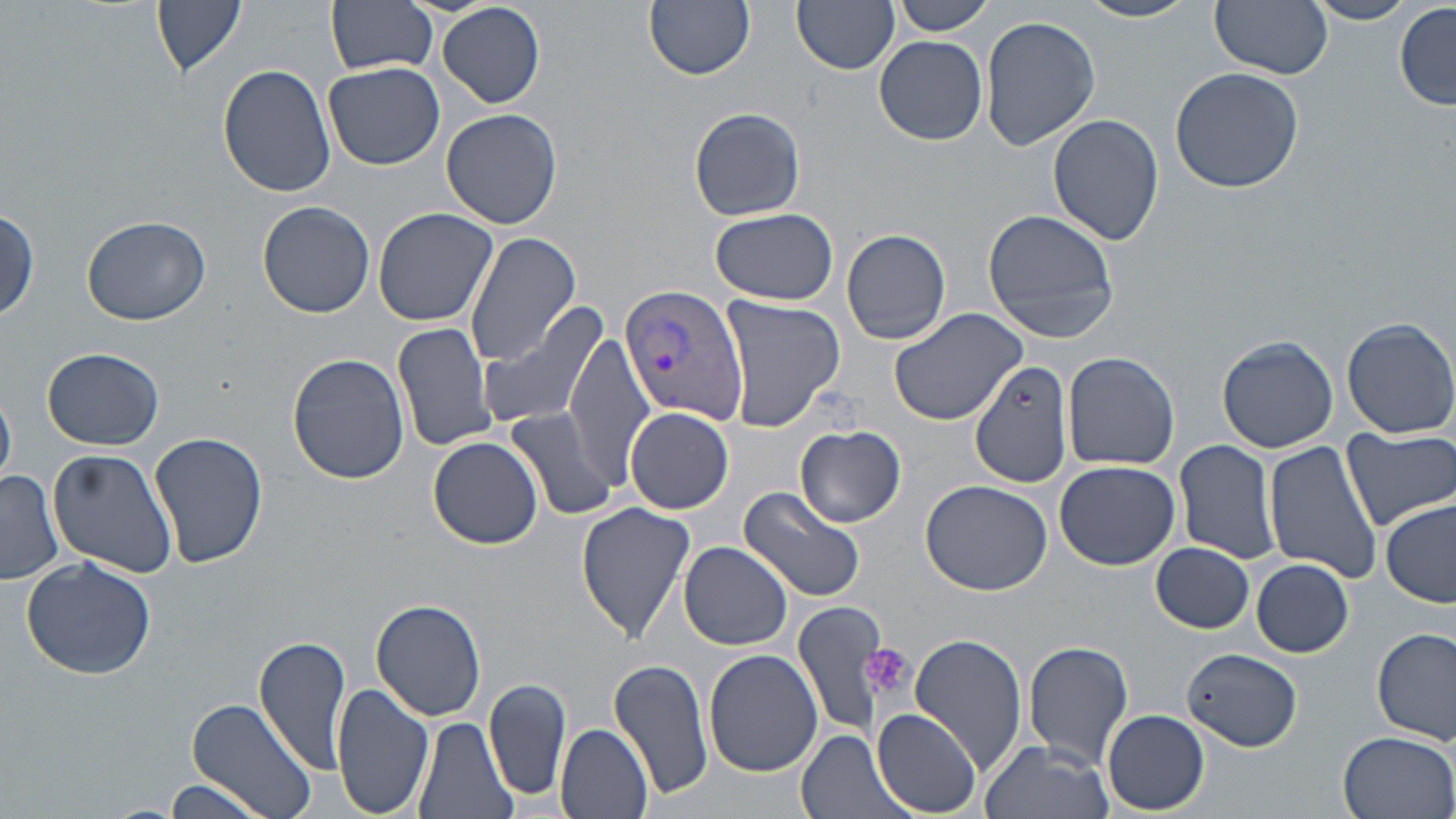

Approximate bounding boxes as named x1/y1/x2/y2 corners in pixels. Plasmodium vivax-infected red blood cell locations: (x1=620, y1=281, x2=750, y2=426). Uninfected red blood cell locations: (x1=151, y1=0, x2=246, y2=80), (x1=326, y1=0, x2=439, y2=76), (x1=644, y1=0, x2=756, y2=80), (x1=792, y1=0, x2=900, y2=75), (x1=887, y1=0, x2=997, y2=36), (x1=1078, y1=0, x2=1202, y2=24), (x1=1210, y1=0, x2=1332, y2=79), (x1=1305, y1=0, x2=1417, y2=25), (x1=1394, y1=3, x2=1455, y2=110), (x1=436, y1=4, x2=546, y2=108), (x1=981, y1=15, x2=1101, y2=151), (x1=875, y1=35, x2=988, y2=145), (x1=323, y1=62, x2=446, y2=170), (x1=218, y1=63, x2=337, y2=197), (x1=1169, y1=65, x2=1304, y2=194), (x1=441, y1=106, x2=561, y2=230), (x1=689, y1=108, x2=805, y2=221), (x1=1047, y1=112, x2=1164, y2=247), (x1=258, y1=201, x2=375, y2=317), (x1=372, y1=206, x2=499, y2=327), (x1=709, y1=206, x2=838, y2=305), (x1=1, y1=208, x2=41, y2=321), (x1=982, y1=209, x2=1118, y2=342), (x1=80, y1=215, x2=211, y2=326), (x1=842, y1=228, x2=952, y2=346), (x1=463, y1=233, x2=582, y2=366), (x1=718, y1=296, x2=846, y2=430), (x1=887, y1=304, x2=1028, y2=428), (x1=479, y1=306, x2=609, y2=431), (x1=1341, y1=316, x2=1456, y2=439), (x1=392, y1=322, x2=499, y2=454), (x1=564, y1=330, x2=655, y2=492), (x1=1216, y1=335, x2=1338, y2=453), (x1=43, y1=347, x2=163, y2=450), (x1=286, y1=351, x2=411, y2=484), (x1=1061, y1=352, x2=1178, y2=471), (x1=971, y1=357, x2=1074, y2=489), (x1=0, y1=383, x2=17, y2=489), (x1=502, y1=405, x2=621, y2=522), (x1=625, y1=406, x2=734, y2=514), (x1=795, y1=426, x2=906, y2=526), (x1=1343, y1=429, x2=1455, y2=530), (x1=151, y1=430, x2=267, y2=569), (x1=429, y1=436, x2=544, y2=550), (x1=1173, y1=438, x2=1281, y2=567), (x1=1262, y1=439, x2=1385, y2=584), (x1=48, y1=448, x2=177, y2=577), (x1=1053, y1=460, x2=1179, y2=570), (x1=0, y1=469, x2=63, y2=586), (x1=921, y1=480, x2=1053, y2=596), (x1=738, y1=484, x2=867, y2=604), (x1=1381, y1=499, x2=1456, y2=609), (x1=576, y1=501, x2=695, y2=643), (x1=680, y1=541, x2=793, y2=651), (x1=1151, y1=542, x2=1254, y2=634), (x1=21, y1=555, x2=157, y2=680), (x1=1249, y1=559, x2=1353, y2=657), (x1=369, y1=598, x2=487, y2=721), (x1=793, y1=598, x2=894, y2=738), (x1=1374, y1=628, x2=1455, y2=746), (x1=911, y1=633, x2=1029, y2=778), (x1=255, y1=635, x2=352, y2=773), (x1=1023, y1=641, x2=1134, y2=766), (x1=1183, y1=647, x2=1303, y2=750), (x1=703, y1=648, x2=823, y2=777), (x1=609, y1=658, x2=716, y2=803), (x1=485, y1=677, x2=572, y2=804), (x1=332, y1=681, x2=434, y2=819), (x1=185, y1=696, x2=318, y2=819), (x1=872, y1=709, x2=983, y2=816), (x1=1102, y1=710, x2=1209, y2=814), (x1=413, y1=717, x2=516, y2=819), (x1=556, y1=723, x2=654, y2=818), (x1=795, y1=728, x2=916, y2=819), (x1=1336, y1=730, x2=1456, y2=818), (x1=980, y1=738, x2=1114, y2=819), (x1=145, y1=779, x2=275, y2=819). Platelet locations: (x1=859, y1=643, x2=913, y2=702). Slide-level diagnosis: Plasmodium vivax. Single field of view. Thin blood smear. Captured at 1000x magnification. Optical microscopy. Image is 1456×819 pixels. May-Grünwald-Giemsa-stained preparation.